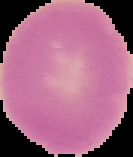 Malaria status: uninfected. Cell region segmented out of the field of view; the surrounding area is masked to black. Image is 133×157 pixels. From a thin blood film.